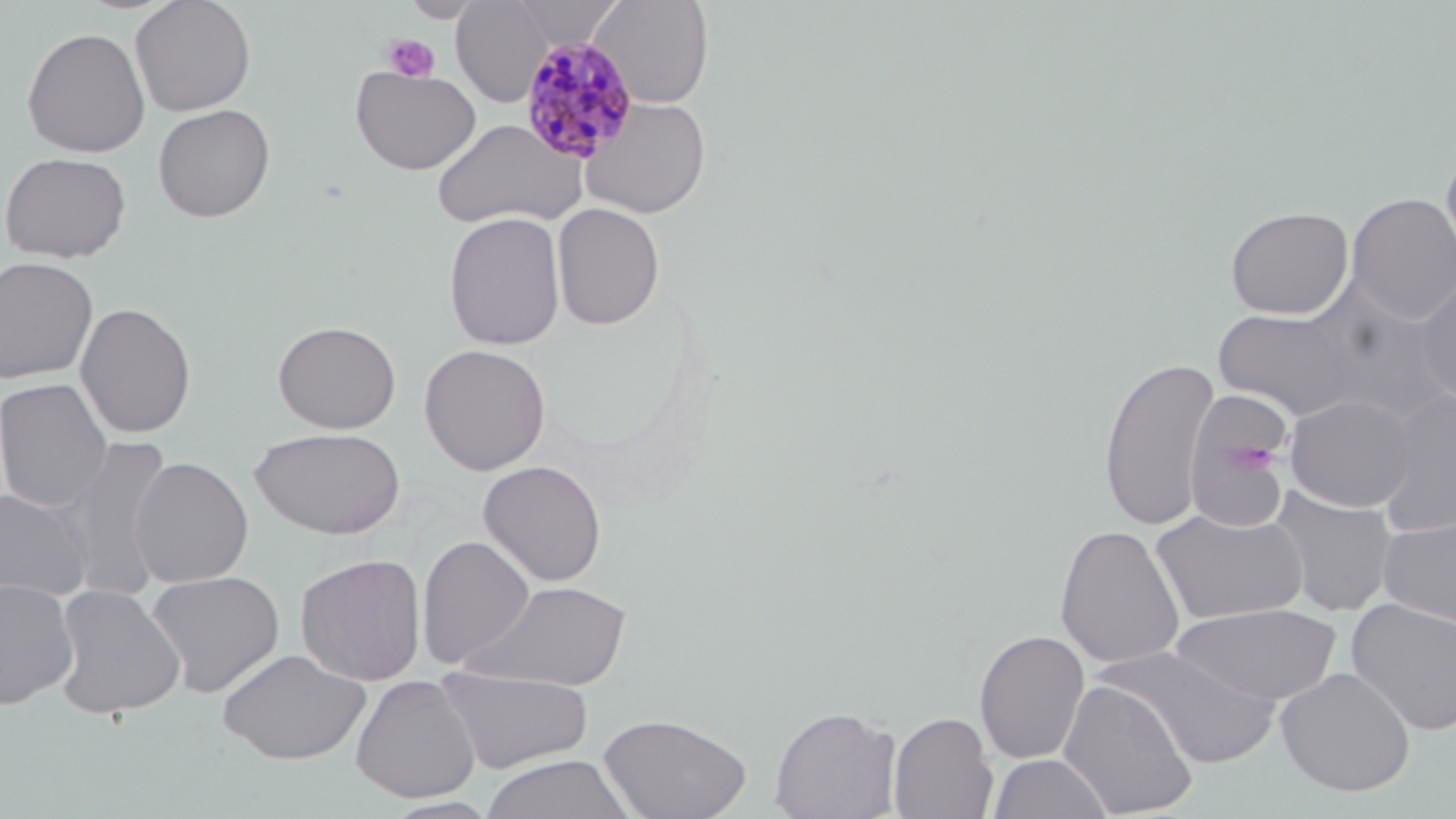
Approximate bounding boxes as (x1,y1)-(x2,y2) corner pairs in pixels. Uninfected red blood cell locations: (129,0)-(257,116), (451,0)-(555,105), (588,0)-(715,109), (504,1)-(624,49), (21,27)-(150,158), (350,65)-(481,175), (579,96)-(712,217), (152,103)-(275,222), (432,118)-(586,230), (1439,147)-(1456,283), (0,151)-(131,263), (1346,192)-(1456,325), (552,202)-(664,330), (1225,205)-(1353,319), (442,212)-(566,351), (0,256)-(99,383), (1414,273)-(1456,404), (1309,291)-(1454,424), (75,302)-(197,439), (1213,305)-(1362,420), (272,320)-(401,433), (418,343)-(551,475), (1098,355)-(1219,531), (0,377)-(114,513), (1375,388)-(1456,537), (1284,393)-(1419,512), (1186,415)-(1290,530), (250,427)-(405,539), (55,434)-(177,598), (129,456)-(253,587), (477,460)-(607,586), (0,487)-(94,602), (1267,487)-(1398,617), (1150,508)-(1309,626), (1377,514)-(1456,630), (1054,523)-(1185,669), (416,534)-(536,669), (295,553)-(427,686), (144,569)-(285,697), (0,577)-(79,710), (462,579)-(633,691), (51,583)-(186,719), (1344,598)-(1456,735), (1171,603)-(1343,706), (974,629)-(1090,764), (1098,644)-(1279,768), (216,648)-(371,764), (434,667)-(595,773), (1275,667)-(1416,797), (350,675)-(481,803), (1058,679)-(1199,818), (768,705)-(901,819), (889,710)-(998,819), (598,711)-(751,819), (987,752)-(1112,819), (479,754)-(636,819), (382,797)-(500,819). Plasmodium malariae-infected red blood cell locations: (518,37)-(639,163). Platelet locations: (381,33)-(441,82), (1236,443)-(1275,476). Slide-level diagnosis: Plasmodium malariae. Captured at 1000x magnification. May-Grünwald-Giemsa stain. Image is 1456×819 pixels. Thin blood smear. Optical microscopy. Single field of view.